Assess the morphology of the erythrocytes.
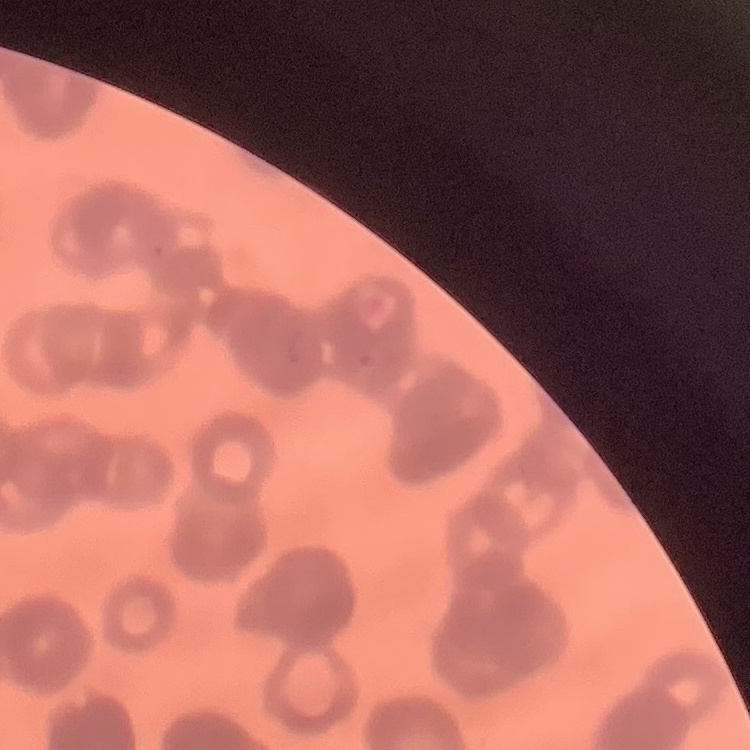

They show rouleaux formation.

stain = Field's or Giemsa
image type = one tile cut from a larger photomicrograph
preparation = thin blood smear